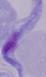

{
  "identification": "trypanosome",
  "magnification": "1000x",
  "modality": "photomicrograph"
}